Give the extent of all Plasmodium falciparum-infected red blood cells.
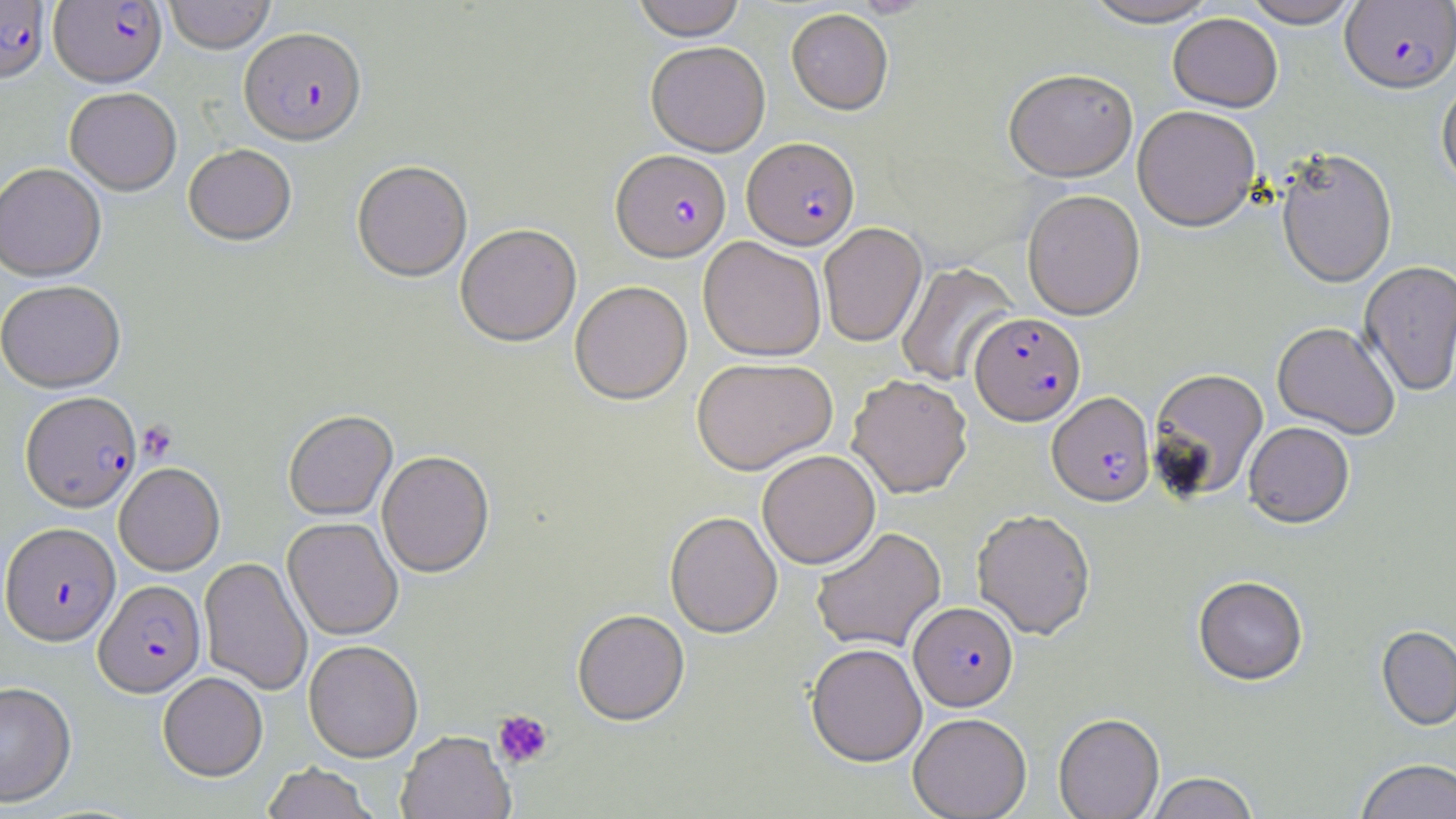

Approximate bounding boxes as (x1,y1)-(x2,y2) corner pairs in pixels.
Plasmodium falciparum-infected red blood cells: (1340,0)-(1456,95), (0,1)-(50,86), (49,1)-(166,90), (238,30)-(367,149), (742,137)-(860,250), (611,149)-(731,262), (970,312)-(1085,425), (1047,392)-(1155,507), (20,394)-(142,514), (1,523)-(121,647), (94,581)-(205,698), (909,602)-(1018,711).

Uninfected red blood cell locations: (164,0)-(275,55), (632,0)-(746,40), (1079,0)-(1224,29), (1240,0)-(1362,28), (786,8)-(893,114), (1168,13)-(1283,113), (646,41)-(770,156), (1003,69)-(1138,182), (1436,78)-(1456,194), (64,90)-(182,198), (1133,106)-(1261,231), (184,146)-(296,248), (1276,149)-(1397,289), (352,162)-(473,283), (0,165)-(106,285), (1022,189)-(1145,320), (818,222)-(927,347), (455,224)-(582,347), (698,236)-(826,361), (1358,261)-(1456,398), (896,262)-(1018,387), (569,280)-(692,405), (0,283)-(127,395), (1272,322)-(1400,440), (692,356)-(838,475), (1149,368)-(1269,501), (848,373)-(973,498), (283,410)-(398,521), (1244,421)-(1354,528), (757,450)-(880,569), (377,451)-(494,578), (114,463)-(225,576), (972,509)-(1096,640), (665,511)-(782,638), (282,518)-(403,641), (811,527)-(946,653), (199,557)-(313,696), (1193,576)-(1308,687), (572,610)-(690,727), (1376,626)-(1456,733), (303,640)-(423,763), (806,643)-(927,767), (158,672)-(268,782), (0,681)-(77,808), (909,712)-(1032,819), (1053,713)-(1164,819), (397,731)-(515,819), (1355,759)-(1456,819), (261,763)-(379,819), (1145,772)-(1260,819). Platelet locations: (139,420)-(177,462), (492,709)-(553,768). Slide-level diagnosis: Plasmodium falciparum. 1000x magnification. May-Grünwald-Giemsa-stained preparation. Image is 1456×819 pixels. Single field of view. Optical microscopy. Thin blood film.